Name the parasite shown.
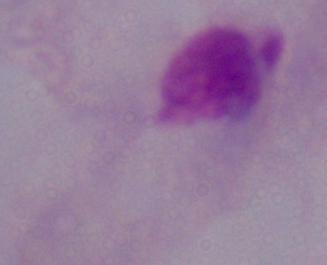
This is a trichomonad.

{
  "magnification": "1000x",
  "modality": "photomicrograph"
}